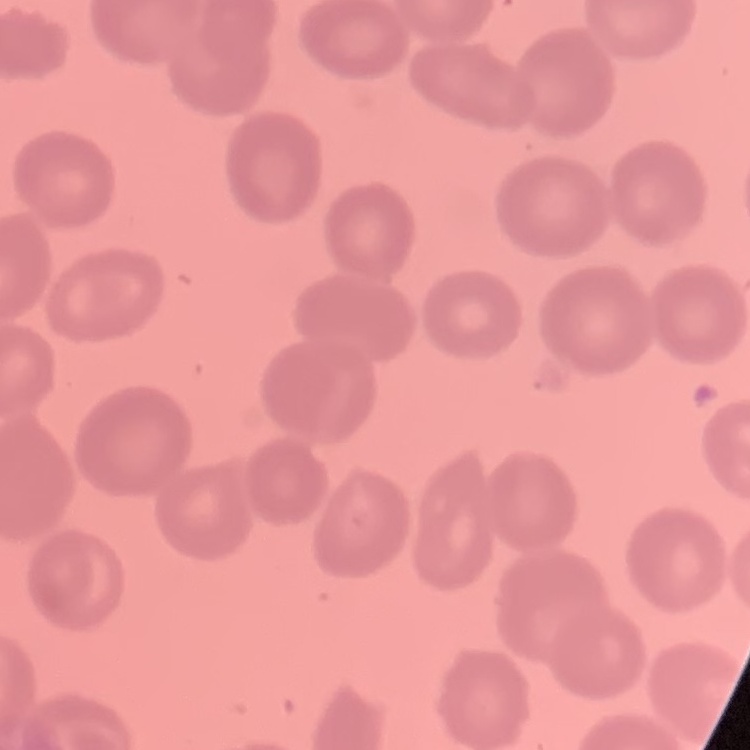
{
  "red_blood_cell_morphology": "no rouleaux formation",
  "preparation": "thin blood film",
  "stain": "Field's or Giemsa",
  "image_type": "one tile cut from a larger photomicrograph"
}